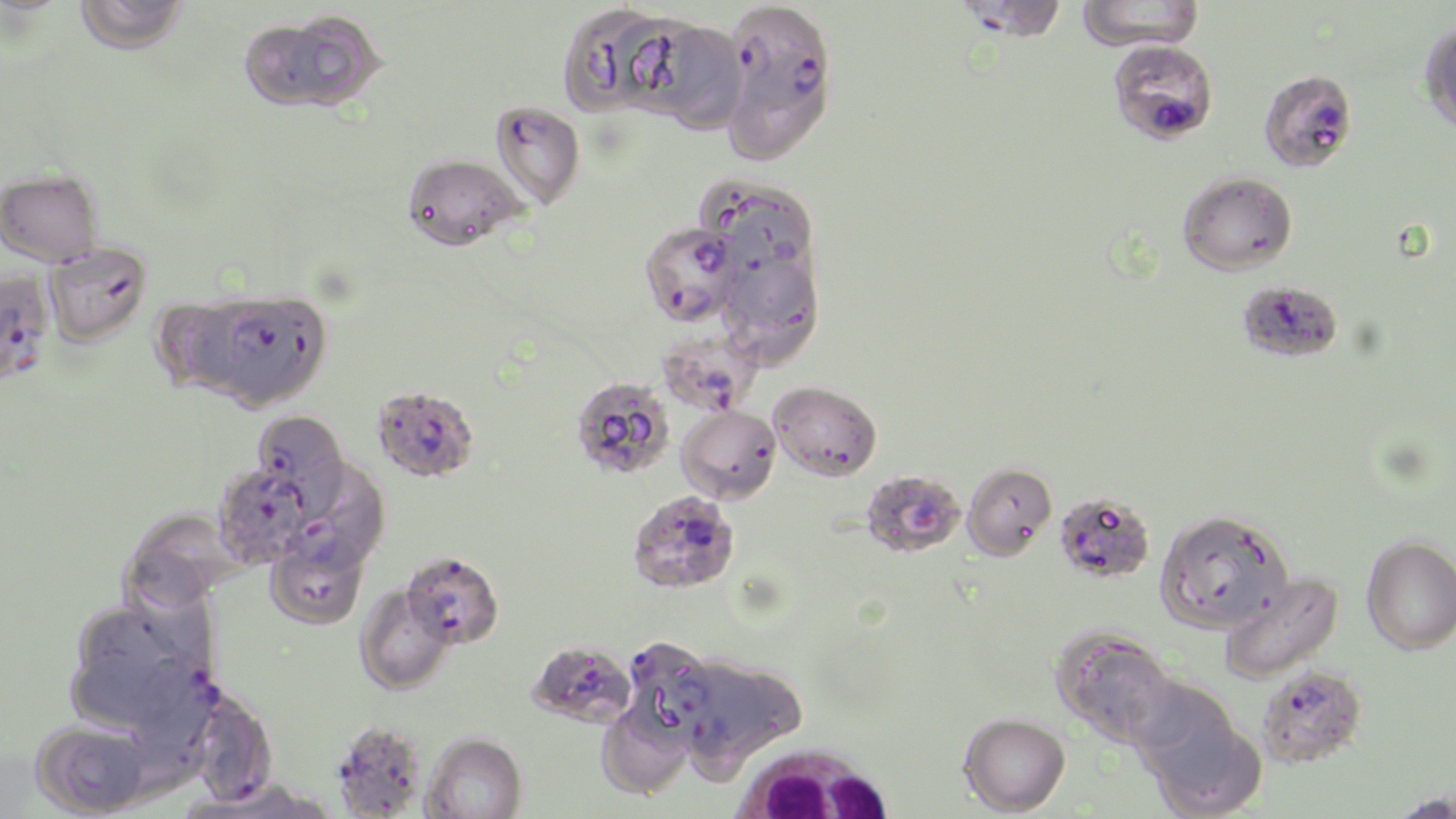

Summary:
  - Coordinate format: approximate bounding boxes as (x1,y1)-(x2,y2) corner pairs in pixels
  - Plasmodium falciparum-infected red blood cell locations: (952,0)-(1070,44), (723,1)-(837,106), (1107,39)-(1218,145), (1258,69)-(1357,173), (490,101)-(585,209), (699,177)-(818,279), (639,221)-(743,327), (0,270)-(55,386), (209,291)-(332,409), (657,326)-(764,416), (371,385)-(480,483), (251,410)-(350,509), (292,461)-(389,571), (213,463)-(315,569), (860,469)-(965,557), (627,490)-(740,593), (1054,492)-(1155,582), (401,551)-(504,649), (625,637)-(717,741), (526,640)-(636,729), (134,656)-(226,755), (1257,664)-(1368,768), (332,721)-(428,819)
  - White blood cell locations: (727,740)-(897,819)
  - Uninfected red blood cell locations: (74,0)-(189,54), (1078,0)-(1205,51), (557,2)-(675,116), (243,10)-(384,113), (628,19)-(748,133), (1419,22)-(1456,134), (718,75)-(831,163), (403,153)-(525,251), (0,168)-(102,266), (1177,171)-(1297,275), (45,241)-(152,346), (722,253)-(823,368), (1237,280)-(1343,363), (151,297)-(250,395), (570,376)-(675,480), (769,381)-(882,480), (676,403)-(781,503), (962,462)-(1057,560), (122,509)-(239,611), (1156,509)-(1293,633), (265,533)-(370,631), (1361,535)-(1456,655), (1218,572)-(1344,685), (355,585)-(456,694), (65,604)-(203,733), (1051,627)-(1177,746), (683,656)-(805,779), (1130,683)-(1263,816), (181,694)-(273,807), (597,705)-(693,800), (959,712)-(1070,815), (32,719)-(153,818), (422,732)-(527,819), (190,777)-(337,819), (1388,791)-(1455,819)
  - Slide-level diagnosis: Plasmodium falciparum
  - Image size: 1456×819 pixels
  - Magnification: 1000x
  - Modality: light microscopy
  - Stain: May-Grünwald-Giemsa
  - Field of view: single
  - Preparation: thin blood smear